Describe the morphology of the red blood cells.
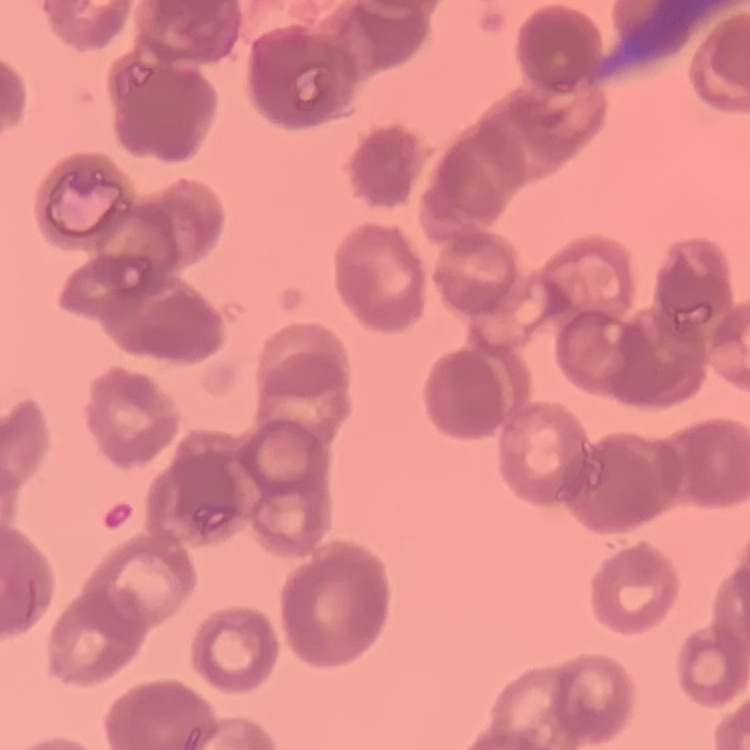
They show rouleaux formation.

Summary:
  - Stain: Field's or Giemsa
  - Preparation: thin peripheral smear
  - Image type: square crop of a larger photomicrograph